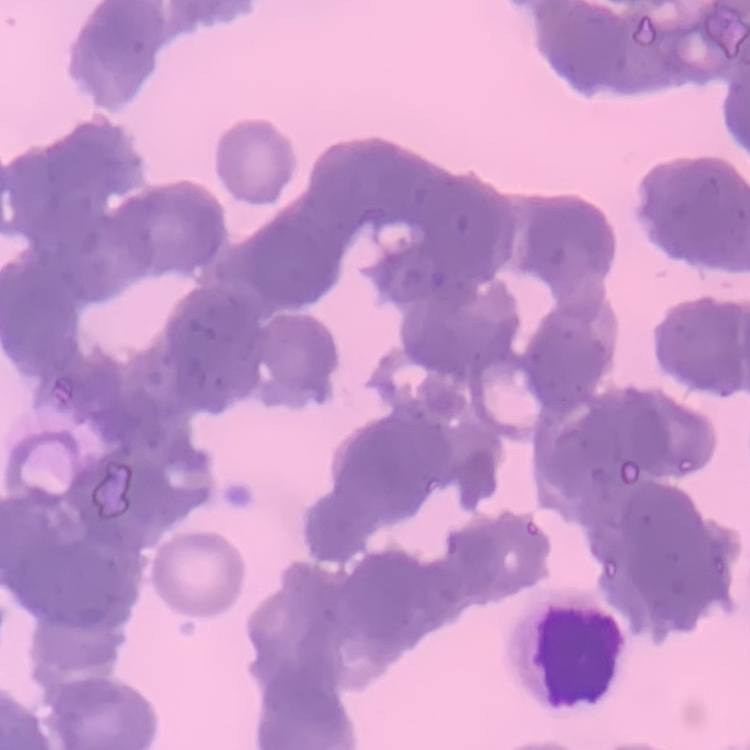
red blood cell morphology = rouleaux formation
stain = Field's or Giemsa
preparation = thin blood smear
image type = square crop of a larger photomicrograph